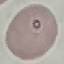

Summary:
  - Result: no malaria parasites seen
  - Image type: automatically extracted cell patch, resized to 64 × 64 pixels
  - Capture: smartphone camera at the microscope eyepiece
  - Preparation: thin blood film
  - Stain: Giemsa